Classify this cell by malaria status.
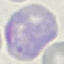

It is parasitized.

capture = smartphone through the microscope eyepiece
stain = Giemsa
image type = cell patch, automatically extracted from a larger field of view and resized to 64 × 64 pixels
preparation = thin blood film